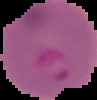

Result: Plasmodium parasites identified. Segmented cell region on a black background. Image is 97×100 pixels. From a thin blood film.